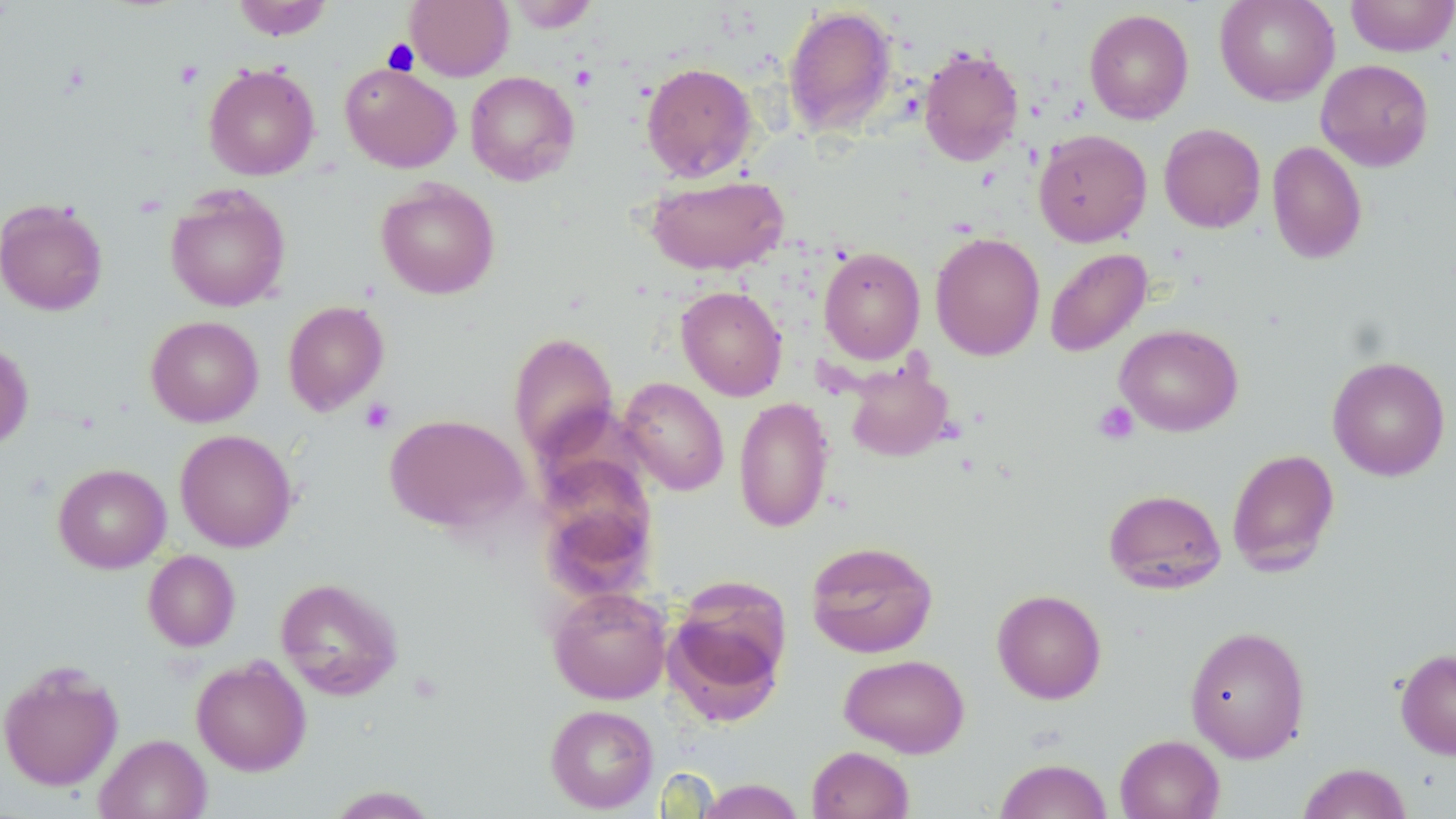
Summary:
  - Coordinate format: approximate bounding boxes as (x1,y1)-(x2,y2) corner pairs in pixels
  - Platelet locations: (382,39)-(419,75), (360,398)-(396,433), (1093,401)-(1139,445)
  - Uninfected red blood cell locations: (232,0)-(333,40), (405,0)-(514,81), (1214,0)-(1340,105), (1345,0)-(1456,57), (505,1)-(599,32), (783,5)-(898,136), (1083,8)-(1194,124), (919,46)-(1024,166), (1315,59)-(1435,171), (641,62)-(758,181), (203,63)-(320,180), (340,63)-(461,173), (465,70)-(580,186), (1158,123)-(1266,233), (1033,129)-(1151,247), (1267,140)-(1367,265), (644,173)-(789,275), (375,179)-(501,299), (165,186)-(291,311), (0,199)-(108,315), (930,231)-(1045,361), (819,247)-(926,363), (1044,248)-(1152,357), (676,285)-(787,400), (282,300)-(389,415), (146,315)-(263,426), (1115,323)-(1243,436), (507,331)-(619,461), (0,340)-(34,451), (1327,356)-(1450,481), (843,362)-(954,462), (618,377)-(729,496), (734,396)-(835,533), (384,413)-(529,534), (174,429)-(297,552), (1226,448)-(1340,576), (537,458)-(657,595), (53,463)-(171,573), (1104,488)-(1226,594), (806,540)-(939,658), (143,550)-(240,651), (275,577)-(404,700), (665,578)-(790,720), (547,586)-(673,704), (992,589)-(1107,704), (1185,625)-(1311,763), (1395,648)-(1456,759), (839,654)-(970,758), (191,655)-(311,776), (0,661)-(124,791), (545,704)-(659,813), (95,733)-(211,819), (1114,734)-(1225,819), (806,745)-(914,819), (994,758)-(1113,819), (1297,762)-(1413,819), (696,778)-(805,819), (324,785)-(441,818)
  - Slide-level diagnosis: no evidence of blood parasites
  - Magnification: 1000x
  - Field of view: single
  - Stain: May-Grünwald-Giemsa
  - Image size: 1456×819 pixels
  - Preparation: thin blood film
  - Modality: light microscopy